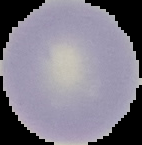 From a thin blood film. Image is 142×145 pixels. Result: no Plasmodium parasites detected. Segmented cell region on a black background.